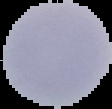
Summary:
  - Preparation: thin blood smear
  - Image size: 112×109 pixels
  - Malaria status: uninfected
  - Image type: segmented cell region with the area outside set to black